Name the parasite shown.
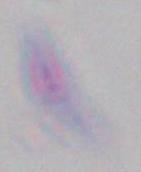
This is Toxoplasma gondii.

{
  "modality": "photomicrograph",
  "magnification": "1000x"
}